Identify the parasite.
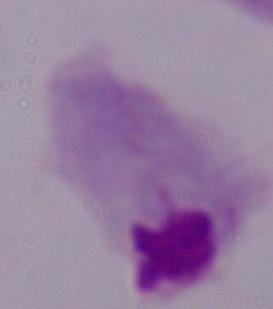

This is a trichomonad.

Captured at 1000x magnification. Micrograph.